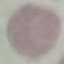
Summary:
  - Malaria status: uninfected
  - Capture: smartphone camera at the microscope eyepiece
  - Preparation: thin blood film
  - Stain: Giemsa
  - Image type: cell patch, automatically extracted from a larger field of view and resized to 64 × 64 pixels